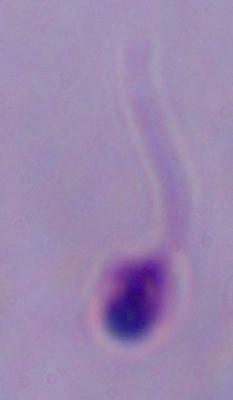

Photomicrograph. A Leishmania parasite is seen. 1000x magnification.